Assess the morphology of the erythrocytes.
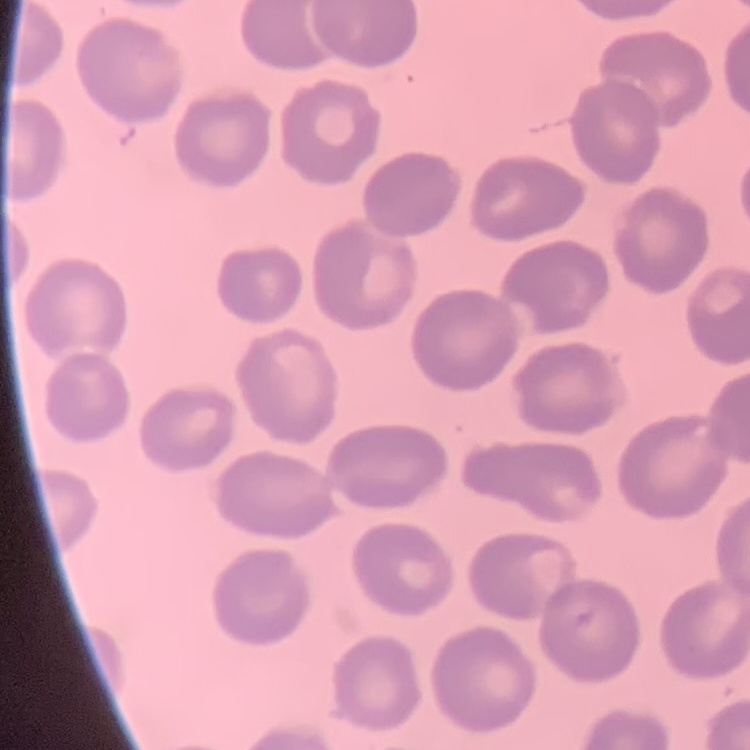
They show no rouleaux formation.

Thin blood smear. Square crop of a larger photomicrograph. Stained with either Field's or Giemsa.